State the blood parasite species.
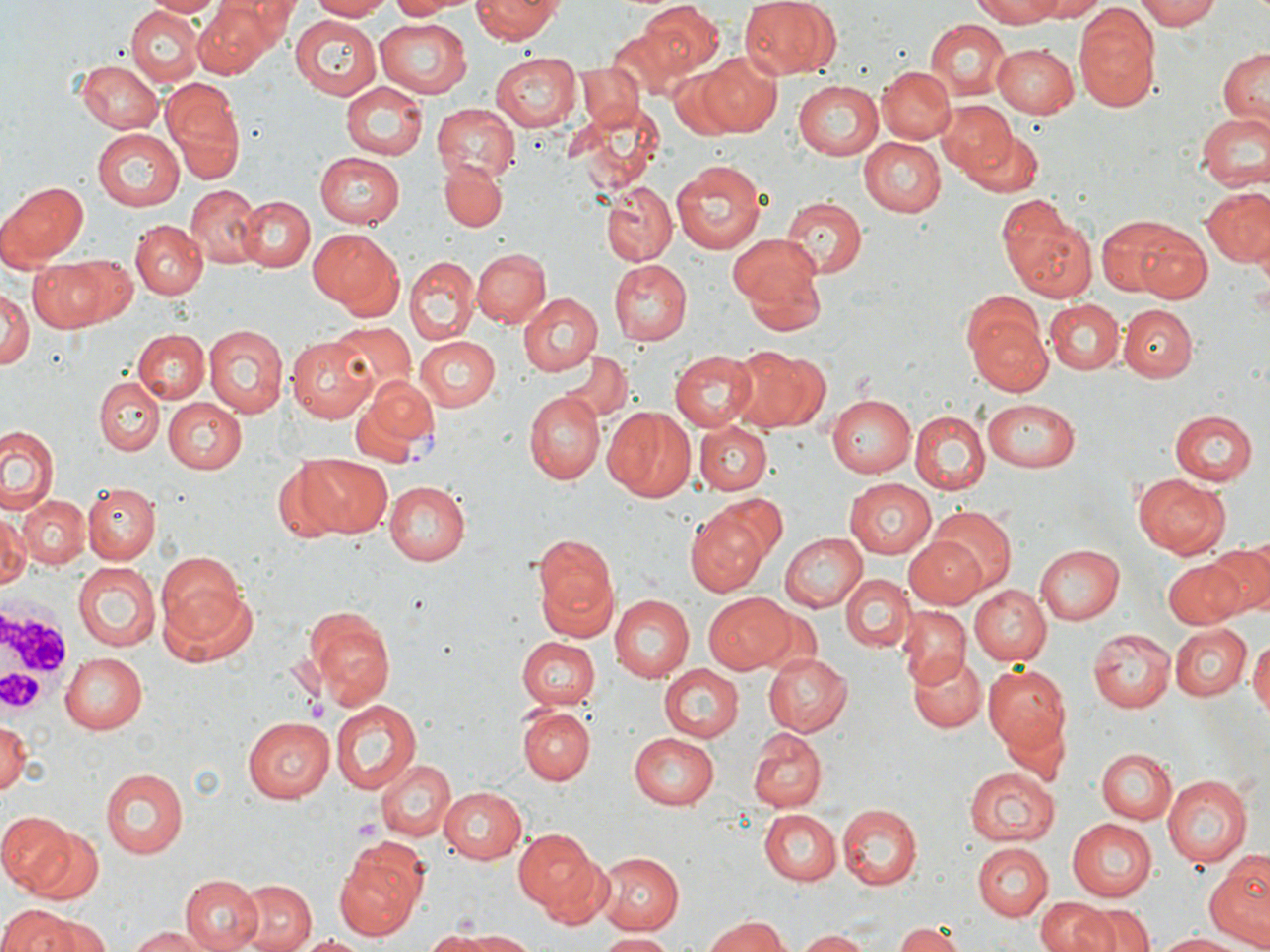
Plasmodium vivax.

Summary:
  - Coordinate format: approximate bounding boxes as [x1, y1, x2, y2] in pixels
  - Plasmodium vivax-infected red blood cell locations: [355, 377, 441, 466]
  - Platelet locations: [353, 815, 382, 847]
  - Uninfected red blood cell locations: [228, 0, 299, 42], [308, 0, 389, 20], [391, 0, 461, 20], [471, 0, 563, 44], [737, 0, 841, 80], [966, 0, 1076, 26], [1031, 0, 1109, 21], [1137, 0, 1219, 32], [145, 1, 224, 19], [193, 1, 280, 76], [637, 2, 723, 77], [125, 5, 203, 85], [1074, 9, 1161, 110], [289, 16, 380, 100], [374, 18, 470, 97], [923, 18, 1011, 100], [607, 25, 690, 99], [992, 42, 1082, 118], [1217, 48, 1270, 125], [488, 52, 579, 131], [698, 53, 784, 136], [76, 61, 161, 133], [574, 64, 643, 133], [877, 65, 955, 146], [665, 66, 751, 142], [341, 80, 427, 159], [794, 80, 883, 159], [160, 82, 244, 182], [936, 101, 1016, 178], [432, 103, 517, 181], [571, 104, 667, 191], [1196, 112, 1270, 191], [92, 129, 184, 210], [958, 129, 1045, 202], [858, 136, 946, 218], [314, 150, 405, 229], [437, 159, 507, 232], [672, 159, 768, 255], [3, 180, 89, 266], [602, 182, 677, 264], [186, 186, 267, 267], [1201, 187, 1270, 268], [235, 195, 316, 272], [780, 196, 868, 278], [996, 200, 1097, 301], [1103, 217, 1211, 301], [131, 220, 206, 299], [306, 227, 401, 315], [729, 237, 827, 332], [472, 250, 552, 329], [29, 253, 126, 332], [405, 257, 477, 344], [608, 260, 691, 345], [0, 289, 32, 369], [518, 293, 602, 377], [1045, 300, 1123, 374], [965, 301, 1051, 395], [1119, 305, 1195, 380], [330, 323, 416, 398], [203, 326, 287, 419], [133, 331, 207, 404], [287, 335, 377, 422], [413, 335, 499, 410], [730, 345, 827, 435], [669, 349, 758, 430], [561, 351, 631, 425], [95, 377, 164, 454], [524, 391, 605, 484], [826, 391, 915, 477], [160, 396, 245, 475], [984, 397, 1085, 471], [604, 409, 695, 501], [910, 409, 989, 494], [1169, 411, 1258, 486], [696, 421, 772, 493], [0, 425, 61, 516], [297, 453, 393, 536], [1134, 471, 1231, 559], [842, 477, 937, 559], [84, 481, 159, 561], [384, 481, 470, 565], [18, 494, 91, 568], [711, 495, 791, 571], [0, 507, 30, 593], [686, 507, 770, 597], [928, 507, 1016, 593], [778, 532, 866, 612], [532, 534, 620, 640], [904, 535, 989, 610], [1207, 542, 1270, 616], [1036, 544, 1124, 624], [155, 554, 246, 645], [1163, 556, 1247, 628], [72, 561, 161, 651], [841, 573, 914, 651], [967, 584, 1051, 665], [161, 586, 260, 669], [703, 593, 794, 672], [610, 594, 694, 681], [302, 604, 396, 709], [896, 607, 970, 686], [757, 611, 818, 674], [1168, 623, 1252, 700], [1089, 629, 1176, 712], [519, 636, 601, 708], [1249, 637, 1270, 724], [58, 651, 146, 733], [762, 652, 851, 735], [906, 654, 986, 733], [981, 663, 1070, 754], [659, 664, 743, 742], [330, 699, 421, 794], [518, 705, 594, 784], [241, 718, 336, 802], [2, 719, 30, 799], [998, 720, 1067, 792], [747, 728, 827, 810], [627, 732, 720, 807], [1097, 747, 1178, 824], [374, 759, 454, 842], [101, 767, 189, 860], [965, 767, 1058, 847], [1161, 775, 1250, 866], [438, 786, 527, 864], [838, 803, 923, 889], [759, 810, 841, 883], [0, 812, 73, 892], [1066, 817, 1156, 902], [512, 828, 607, 918], [26, 829, 104, 901], [972, 842, 1049, 919], [594, 851, 684, 934], [333, 852, 425, 939], [1205, 852, 1270, 949], [180, 874, 265, 952], [230, 878, 314, 952], [1034, 897, 1111, 952], [0, 903, 92, 952], [1082, 903, 1153, 952], [27, 914, 111, 951], [706, 915, 792, 951], [894, 922, 965, 951], [126, 927, 213, 952], [428, 929, 544, 949], [797, 930, 875, 952], [1152, 930, 1254, 950], [293, 932, 376, 951], [598, 932, 675, 951]
  - White blood cell locations: [0, 605, 81, 712]
  - Stain: May-Grünwald-Giemsa
  - Magnification: 1000x
  - Field of view: single
  - Preparation: thin blood smear
  - Modality: light microscopy
  - Image size: 1270×952 pixels